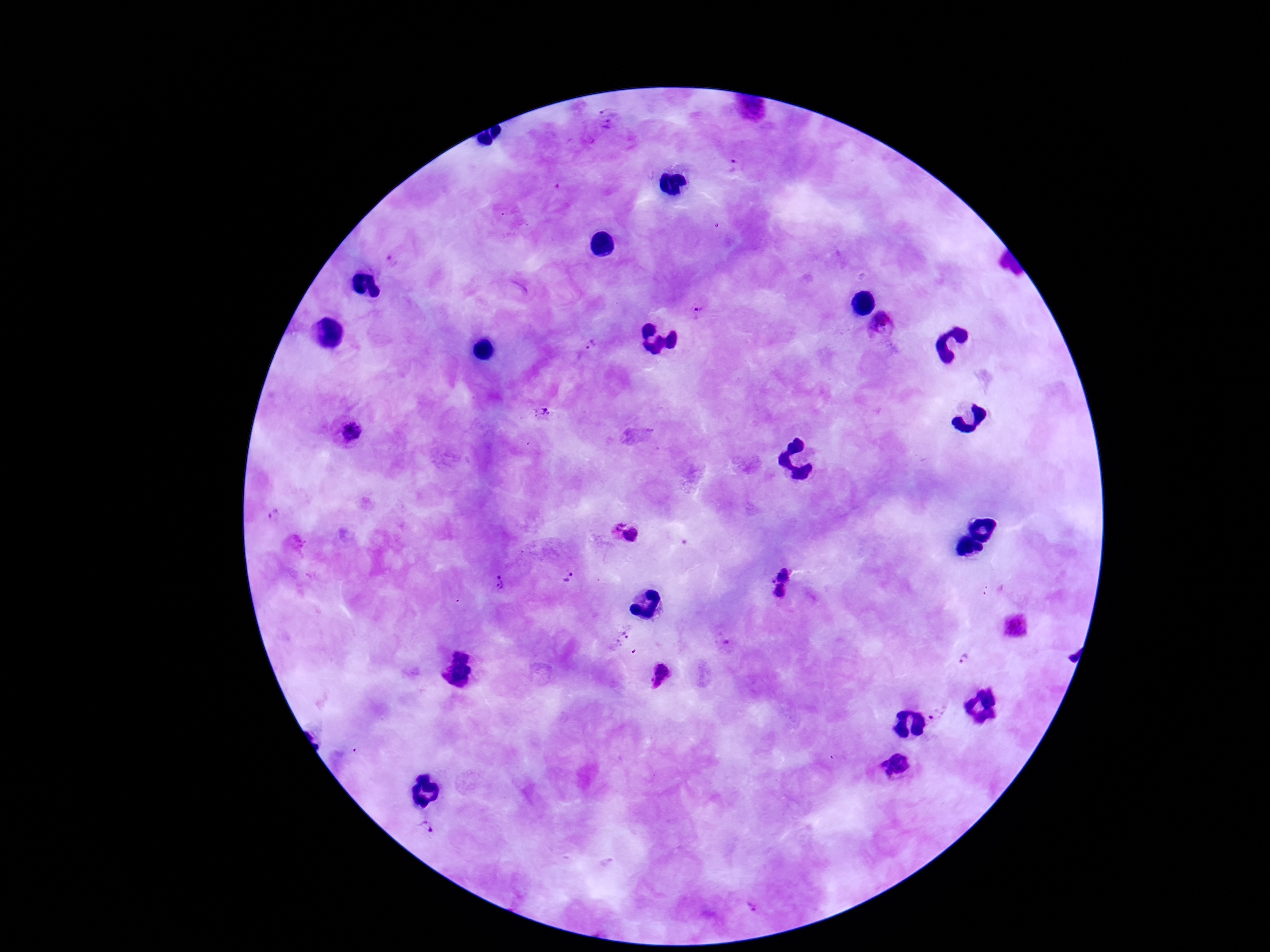
Approximate centers as {x, y} in pixels.
Summary:
  - Plasmodium parasite locations: {609, 120}, {733, 168}, {393, 262}, {697, 313}, {882, 328}, {595, 344}, {544, 413}, {350, 431}, {276, 516}, {624, 533}, {296, 547}, {785, 572}, {570, 578}, {769, 581}, {502, 583}, {780, 592}, {1015, 626}, {621, 637}, {964, 657}, {662, 674}, {941, 716}, {902, 769}, {427, 827}, {752, 907}
  - Capture: smartphone camera through the microscope eyepiece
  - Preparation: thick blood film
  - Magnification: 100x
  - Stain: Giemsa
  - Field of view: one from this slide
  - Patient malaria status: positive
  - Image size: 1270×952 pixels